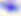
Summary:
  - Identification: Toxoplasma gondii
  - Magnification: 400x
  - Modality: photomicrograph